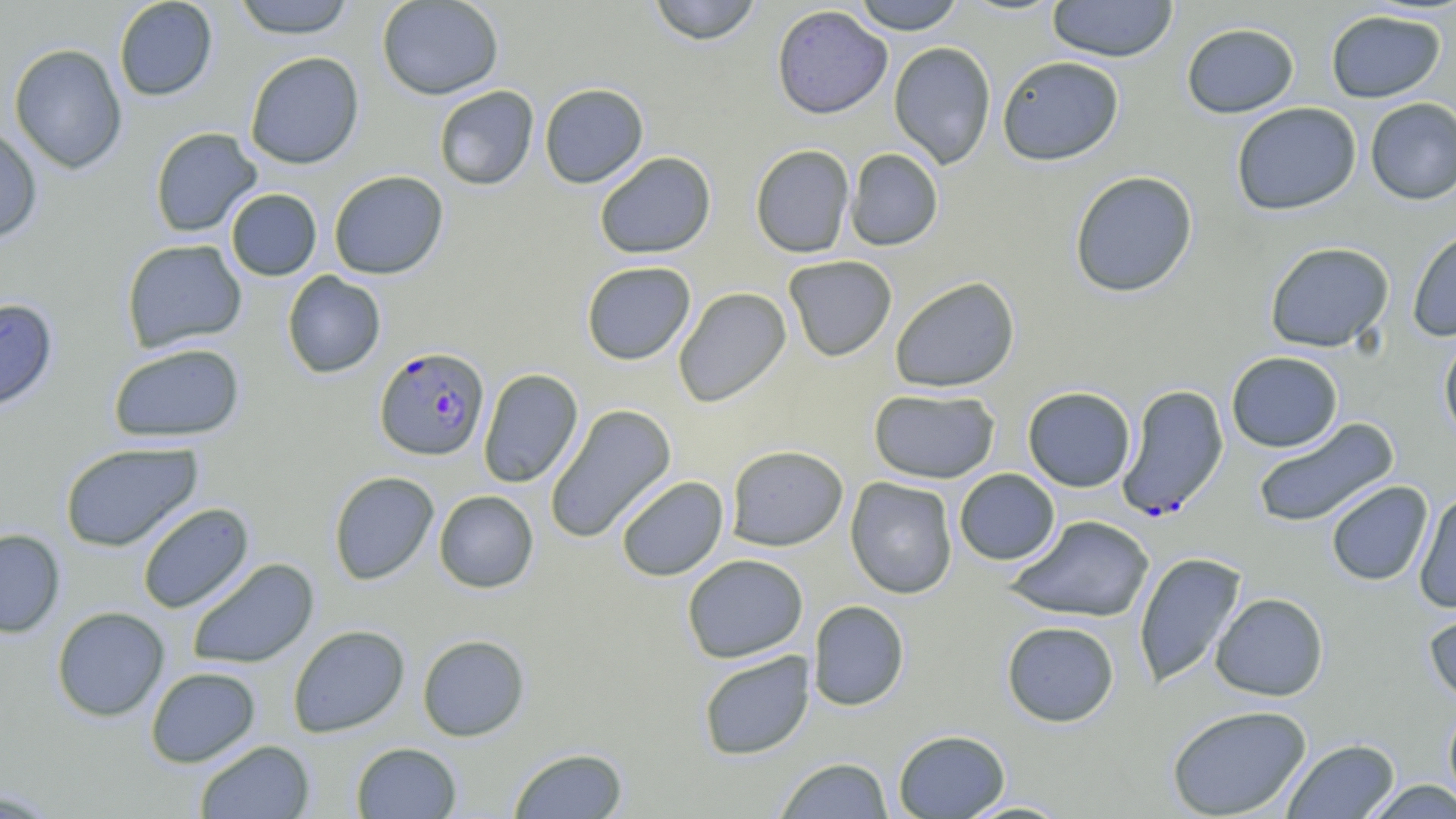
Approximate bounding boxes as [x1, y1, x2, y2] in pixels. Plasmodium falciparum-infected red blood cell locations: [374, 346, 490, 461], [1116, 383, 1229, 520]. Uninfected red blood cell locations: [113, 0, 218, 101], [231, 0, 357, 38], [376, 0, 503, 100], [647, 0, 763, 46], [852, 0, 966, 34], [1046, 0, 1178, 62], [771, 4, 892, 119], [1325, 9, 1446, 103], [1181, 22, 1300, 118], [888, 41, 996, 169], [9, 43, 127, 175], [244, 51, 365, 169], [996, 55, 1124, 166], [539, 82, 649, 188], [433, 86, 539, 190], [1365, 97, 1456, 205], [1231, 102, 1362, 216], [0, 124, 43, 243], [149, 127, 263, 237], [750, 144, 855, 258], [845, 148, 943, 251], [594, 151, 716, 259], [328, 170, 449, 280], [1069, 170, 1198, 297], [225, 188, 322, 281], [1407, 225, 1456, 341], [121, 238, 247, 353], [1264, 241, 1395, 353], [783, 255, 897, 361], [581, 261, 696, 365], [282, 271, 386, 378], [890, 276, 1020, 393], [673, 287, 792, 407], [0, 297, 58, 413], [1438, 333, 1456, 446], [107, 342, 246, 443], [1226, 351, 1343, 452], [478, 368, 583, 488], [1022, 386, 1136, 492], [868, 388, 1000, 484], [545, 403, 677, 544], [1251, 417, 1399, 529], [60, 440, 203, 552], [726, 444, 848, 551], [954, 468, 1060, 565], [328, 471, 440, 585], [615, 475, 729, 581], [845, 477, 958, 599], [1325, 481, 1433, 586], [434, 490, 538, 593], [1414, 490, 1456, 614], [136, 502, 254, 614], [1007, 515, 1155, 623], [0, 528, 65, 638], [1133, 552, 1247, 688], [682, 554, 808, 662], [187, 558, 320, 669], [1210, 592, 1329, 701], [808, 600, 910, 711], [1423, 603, 1456, 707], [51, 606, 170, 721], [1001, 620, 1120, 727], [288, 624, 409, 737], [417, 634, 530, 741], [697, 650, 815, 760], [145, 667, 260, 767], [1442, 700, 1456, 811], [1167, 704, 1312, 818], [893, 729, 1011, 818], [1282, 739, 1400, 818], [194, 740, 315, 818], [351, 742, 462, 818], [508, 747, 629, 818], [774, 757, 894, 818], [1362, 780, 1456, 818], [0, 788, 62, 818], [956, 800, 1075, 818]. Slide-level diagnosis: Plasmodium falciparum. Thin blood film. Single field of view. Optical microscopy. Image is 1456×819 pixels. 1000x magnification. May-Grünwald-Giemsa-stained preparation.